Identify the preparation type.
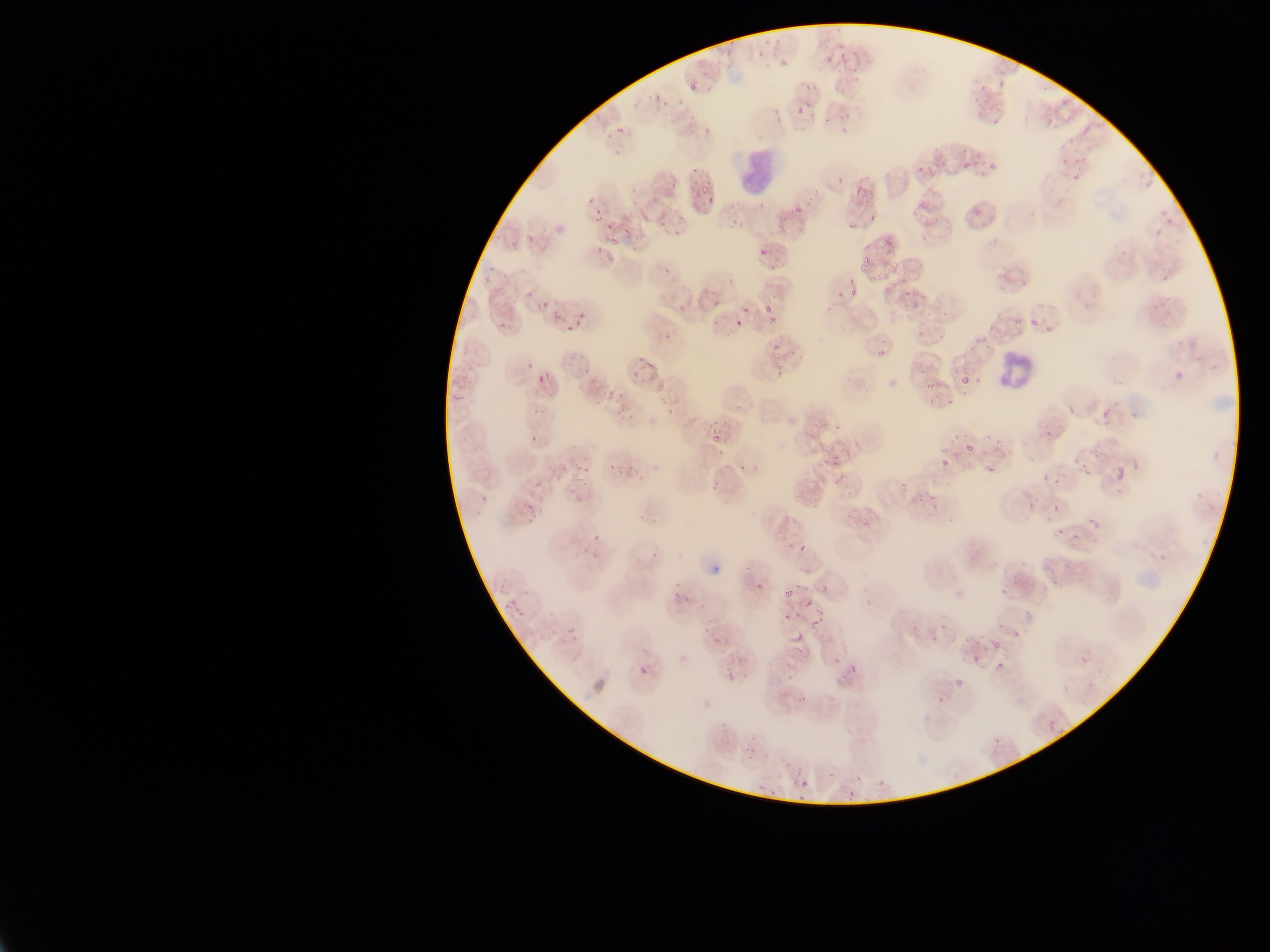
Thin blood smear.

capture = mobile-phone photograph through a microscope
image size = 1270×952 pixels
country = Ghana
malaria parasite locations = approximate bounding boxes as left top right bottom in pixels (subset; some below the resolvable size): 779 60 787 65; 691 83 696 91; 657 94 660 103; 1081 124 1090 135; 841 127 850 132; 962 162 968 170; 839 175 843 183; 858 186 862 197; 595 206 600 214; 596 213 603 222; 869 214 877 220; 847 223 855 227; 623 227 632 233; 883 239 891 247; 861 264 869 269; 884 288 892 294; 918 293 924 301; 744 305 749 315; 764 305 771 313; 735 321 743 326; 566 325 574 330; 918 328 923 337; 663 334 672 340; 646 362 654 369; 1174 371 1181 382; 961 376 969 383; 926 383 934 387; 451 394 467 399; 1101 406 1110 421; 667 407 676 415; 1116 464 1124 481; 1083 470 1092 475; 1043 474 1049 482; 1053 503 1060 511; 785 589 795 596; 804 603 812 607; 811 620 819 625; 567 628 576 633; 1015 629 1019 637; 791 634 803 643; 1081 655 1086 664; 995 660 1002 668; 956 678 964 689; 1048 719 1055 732 | approximate x y pixel centers of objects too small to bound: 842 44; 760 54; 829 60; 852 70; 856 79; 808 86; 666 103; 800 110; 827 121; 620 130; 919 168; 695 170; 928 170; 705 189; 711 200; 870 204; 797 208; 614 240; 762 250; 865 259; 771 267; 668 269; 877 276; 850 281; 853 293; 544 305; 582 314; 775 346; 641 359; 634 374; 539 377; 659 388; 824 425; 1048 433; 817 435; 535 439; 716 439; 819 444; 832 447; 823 451; 945 462; 1077 462; 987 467; 578 469; 992 470; 1056 480; 537 484; 1090 520; 1059 531; 596 537; 585 549; 801 549; 804 587; 998 644; 836 661; 853 669; 804 785; 851 794
leukocyte locations = approximate bounding boxes as left top right bottom in pixels: 734 149 778 192; 998 352 1033 390
field of view = single